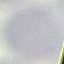

Summary:
  - Malaria status: uninfected
  - Preparation: thin blood smear
  - Capture: smartphone camera at the microscope eyepiece
  - Stain: Giemsa
  - Image type: automatically extracted cell patch, resized to 64 × 64 pixels